Assess the morphology of the erythrocytes.
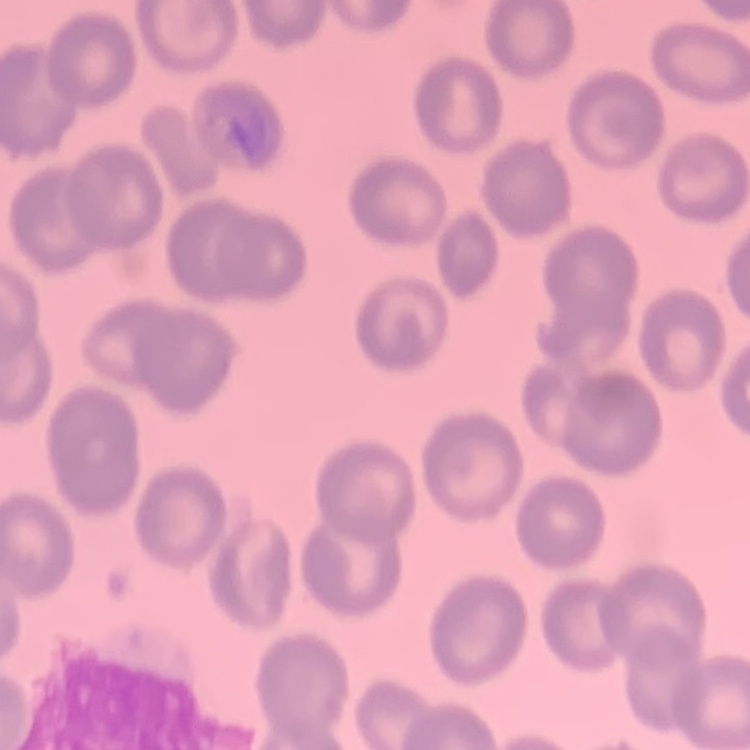
No rouleaux formation.

Summary:
  - Stain: Field's or Giemsa
  - Preparation: thin peripheral smear
  - Image type: one tile cut from a larger photomicrograph